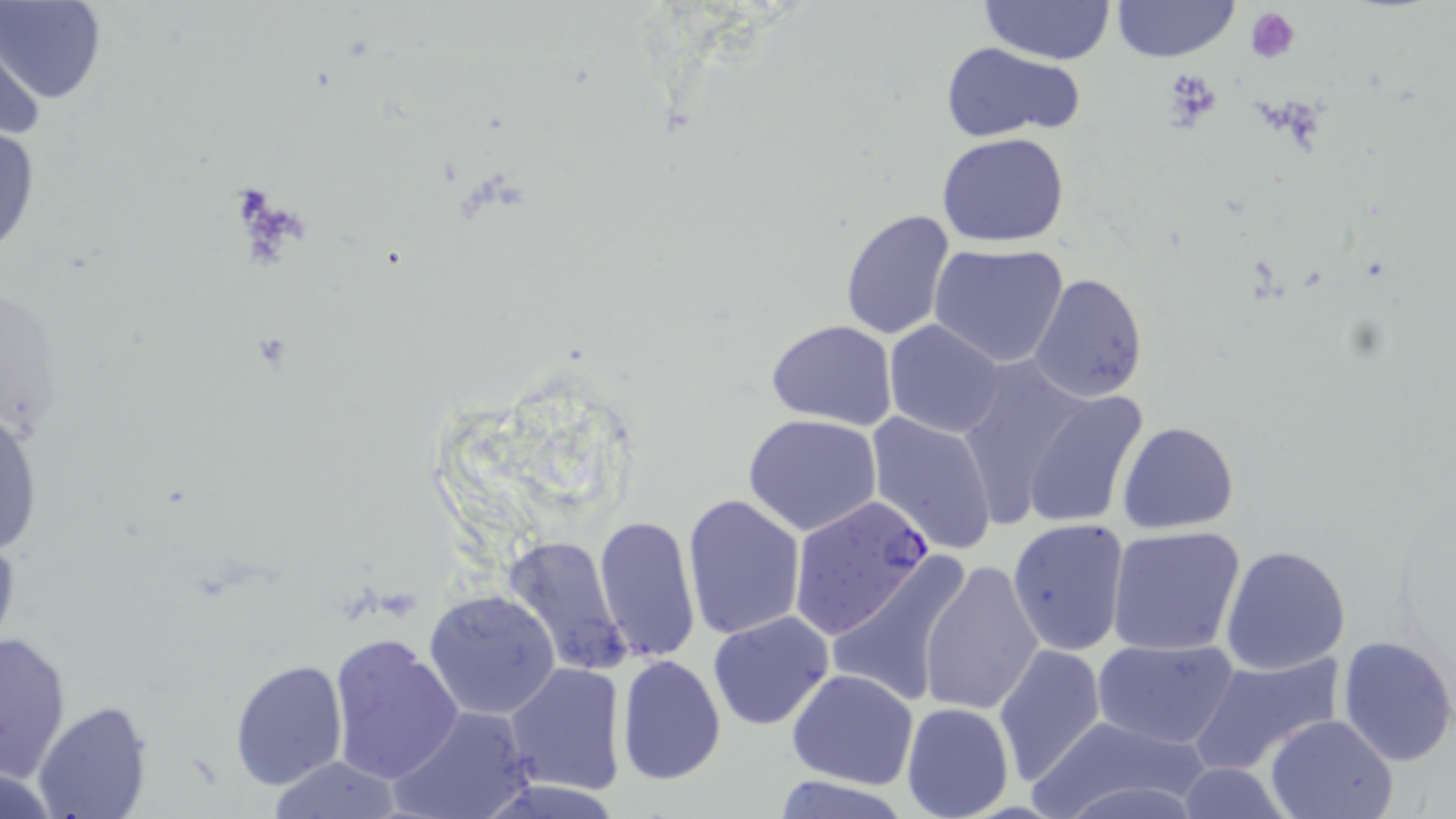
Summary:
  - Coordinate format: approximate bounding boxes as (x1,y1)-(x2,y2) corner pairs in pixels
  - Plasmodium falciparum-infected red blood cell locations: (786,495)-(936,642)
  - Platelet locations: (1246,6)-(1301,63), (1160,67)-(1225,134)
  - Uninfected red blood cell locations: (1,0)-(106,106), (1111,0)-(1239,64), (978,1)-(1115,66), (2,23)-(47,157), (939,41)-(1087,143), (0,114)-(41,265), (937,131)-(1070,246), (839,209)-(956,341), (928,242)-(1069,366), (1027,271)-(1147,403), (765,320)-(897,429), (883,321)-(1006,438), (953,354)-(1095,523), (1019,390)-(1147,530), (0,398)-(44,559), (866,410)-(999,555), (743,413)-(883,536), (1116,420)-(1240,534), (680,493)-(805,640), (593,514)-(700,663), (1006,518)-(1130,657), (1107,526)-(1247,657), (503,534)-(631,674), (1220,544)-(1351,676), (826,552)-(975,709), (917,559)-(1044,716), (424,589)-(563,721), (707,611)-(834,731), (1,630)-(73,779), (327,634)-(463,783), (1335,634)-(1456,766), (1093,635)-(1240,751), (993,642)-(1107,785), (1189,651)-(1346,774), (615,654)-(727,785), (228,658)-(347,791), (504,663)-(625,795), (787,669)-(918,788), (32,700)-(152,819), (901,701)-(1013,819), (389,705)-(534,819), (1026,714)-(1216,819), (1266,714)-(1397,819), (264,756)-(407,817), (1170,763)-(1294,818), (767,774)-(920,819)
  - Slide-level diagnosis: Plasmodium falciparum
  - Magnification: 1000x
  - Image size: 1456×819 pixels
  - Field of view: single
  - Preparation: thin blood film
  - Stain: May-Grünwald-Giemsa
  - Modality: optical microscopy